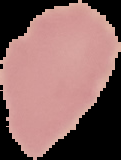
Summary:
  - Image type: segmented cell region with the area outside set to black
  - Image size: 121×160 pixels
  - Preparation: thin blood smear
  - Result: negative for malaria parasites